Outline each Plasmodium falciparum parasite and classify it by life-cycle stage.
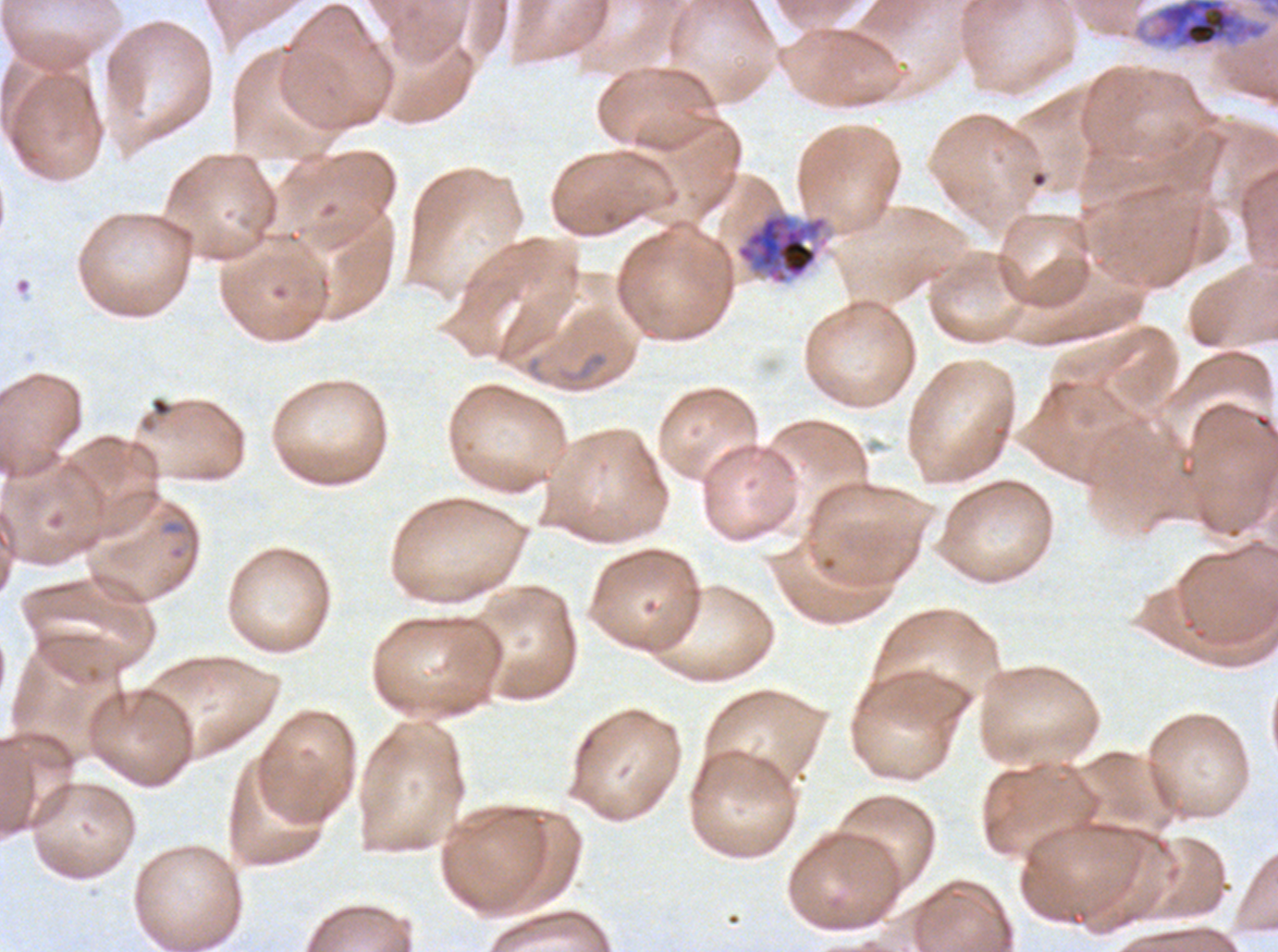

Approximate bounding boxes as {x1, y1, x2, y2} in pixels.
Rings: {560, 350, 608, 384}, {162, 519, 186, 535}.
Early schizonts: {1132, 0, 1272, 50}, {735, 211, 829, 286}.
No late-ring/early-trophozoite forms, mid trophozoites, late trophozoites, late schizonts, segmenters, or gametocytes observed.

One sub-image of a larger composite. Thin blood smear. Life-cycle stages observed: ring, early schizont. Giemsa stain. Image is 1278×952 pixels. Plasmodium falciparum from a patient in The Gambia, cultured ex vivo for 24 to 48 hours.